Report the malaria status of this cell.
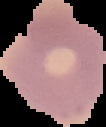

Uninfected.

preparation = thin blood film
image size = 106×127 pixels
image type = segmented cell region with the area outside set to black